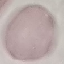

Summary:
  - Result: no malaria parasites seen
  - Stain: Giemsa
  - Capture: smartphone camera at the microscope eyepiece
  - Preparation: thin blood smear
  - Image type: cell patch, automatically extracted from a larger field of view and resized to 64 × 64 pixels